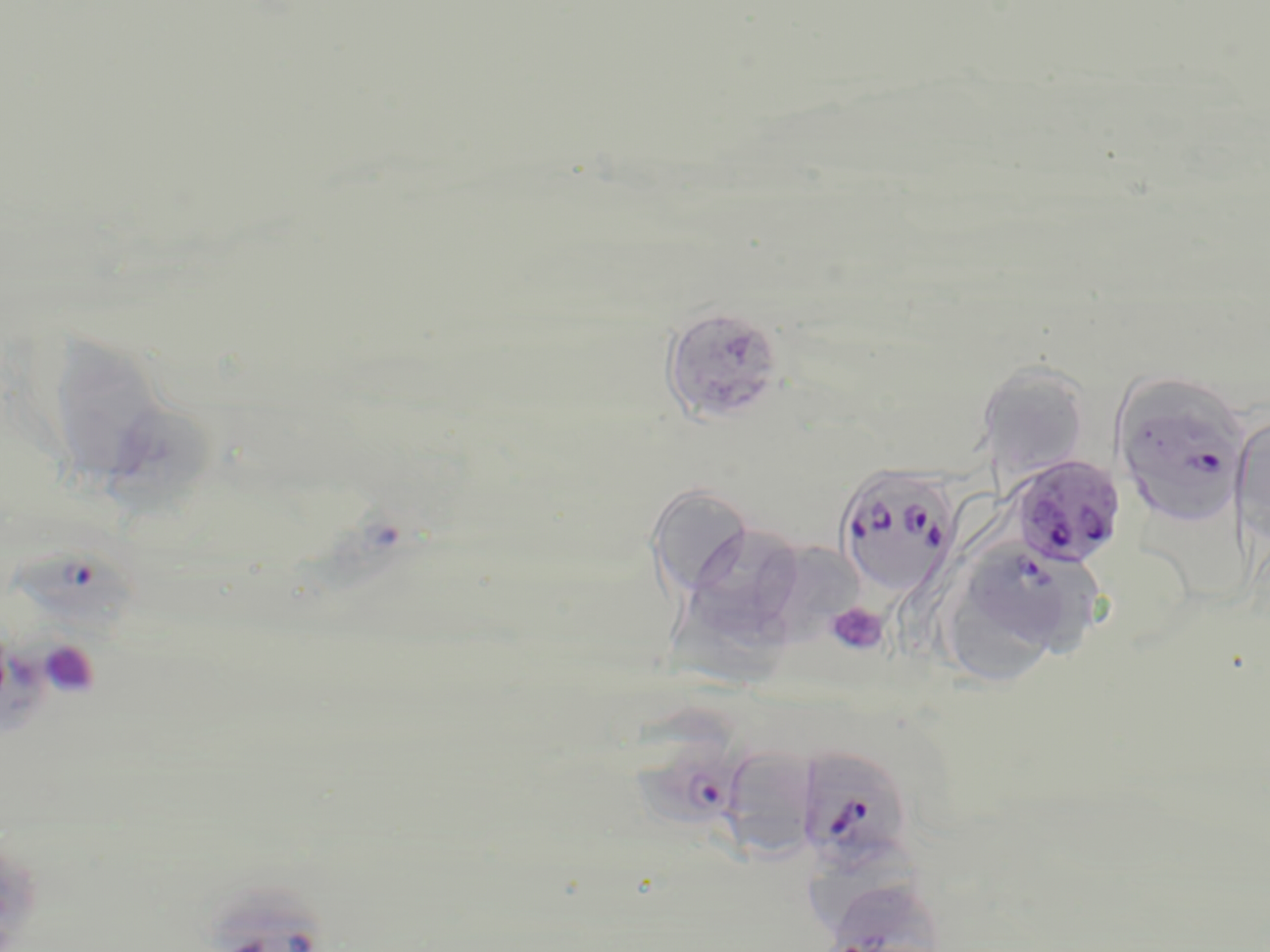

plasmodium_falciparum_infected_red_blood_cell_locations: 'approximate bounding boxes as (x1,y1)-(x2,y2) corner pairs in pixels: (660,305)-(786,426), (1113,377)-(1249,528), (1011,455)-(1124,569), (835,465)-(959,598), (12,538)-(139,637), (956,541)-(1075,661), (631,707)-(747,820), (795,745)-(915,874), (832,888)-(944,952)'
slide_level_diagnosis: Plasmodium falciparum
stain: May-Grünwald-Giemsa
field_of_view: single
image_size: 1270×952 pixels
preparation: thin blood film
magnification: 1000x
modality: optical microscopy
platelet_locations: 'approximate bounding boxes as (x1,y1)-(x2,y2) corner pairs in pixels: (825,601)-(889,657), (37,638)-(100,699)'
uninfected_red_blood_cell_locations: 'approximate bounding boxes as (x1,y1)-(x2,y2) corner pairs in pixels: (59,329)-(164,474), (977,360)-(1090,479), (107,403)-(220,528), (1231,414)-(1270,547), (646,482)-(754,599), (693,517)-(804,640), (774,542)-(868,638), (672,604)-(796,696), (733,749)-(821,862), (807,839)-(925,933)'